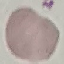
Result: no malaria parasites detected. Giemsa stain. Acquired by smartphone through the microscope eyepiece. Cell patch, automatically extracted from a larger field of view and resized to 64 × 64 pixels. Thin blood film.